State the blood parasite species.
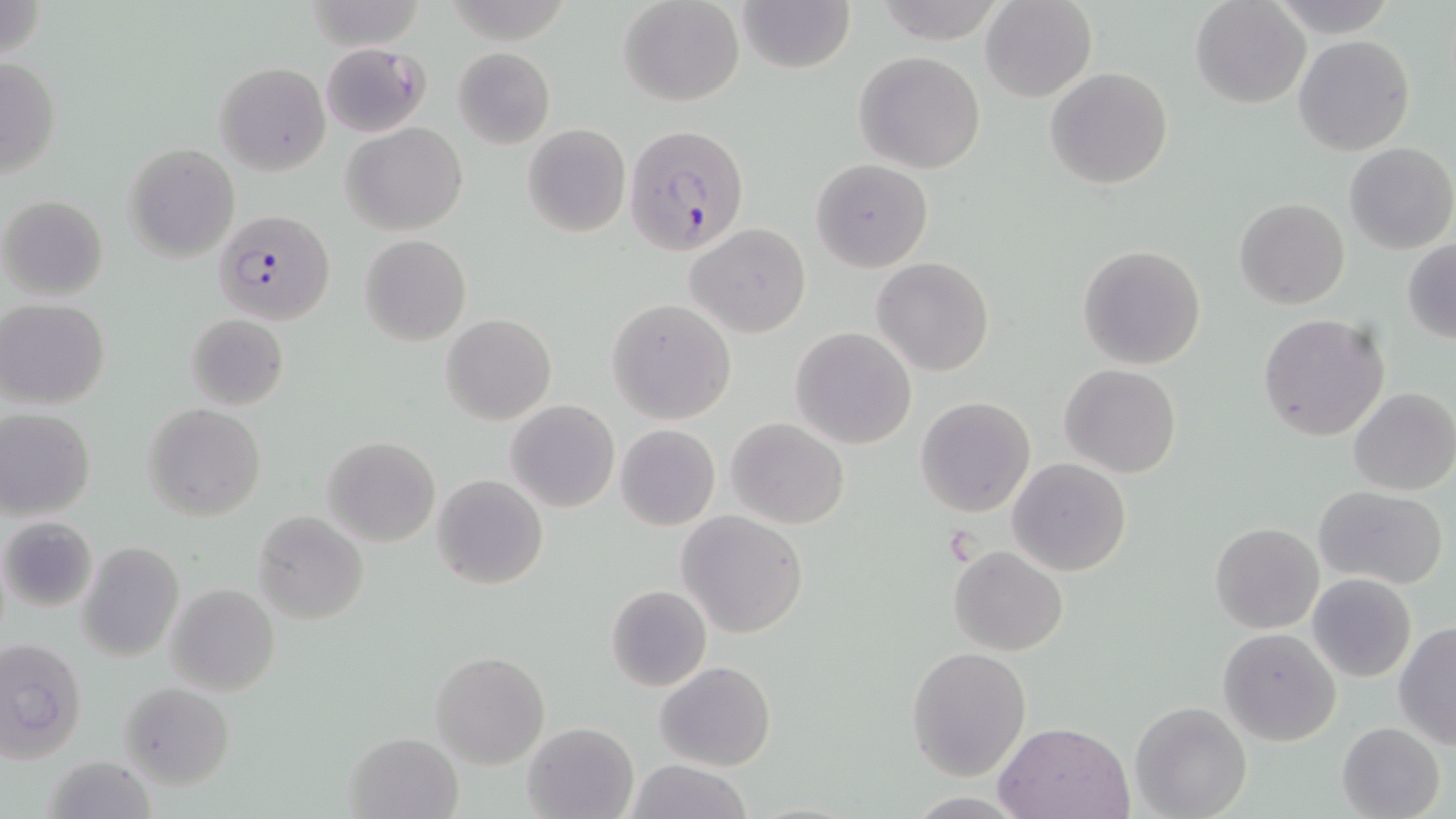
Plasmodium falciparum.

preparation = thin blood smear
Plasmodium falciparum-infected red blood cell locations = approximate bounding boxes as (x1,y1)-(x2,y2) corner pairs in pixels: (623,123)-(750,255), (216,210)-(334,325)
stain = May-Grünwald-Giemsa
image size = 1456×819 pixels
magnification = 1000x
modality = optical microscopy
field of view = one of a larger specimen
uninfected red blood cell locations = approximate bounding boxes as (x1,y1)-(x2,y2) corner pairs in pixels: (618,0)-(745,106), (736,0)-(855,73), (981,0)-(1098,102), (1190,0)-(1311,109), (1264,1)-(1403,35), (304,2)-(427,50), (1293,35)-(1414,156), (321,41)-(431,138), (453,47)-(555,148), (854,51)-(985,173), (0,56)-(61,177), (214,62)-(331,174), (1045,65)-(1173,189), (340,122)-(469,235), (522,124)-(630,237), (1343,141)-(1456,254), (123,144)-(240,262), (812,158)-(932,271), (1,195)-(108,301), (1233,198)-(1351,310), (687,223)-(810,338), (359,234)-(471,346), (1402,239)-(1456,343), (1077,243)-(1205,369), (872,257)-(995,376), (609,298)-(735,424), (1,299)-(110,410), (185,312)-(289,410), (1258,313)-(1390,441), (441,314)-(556,425), (790,327)-(916,449), (1060,363)-(1182,478), (1348,387)-(1456,496), (914,396)-(1036,516), (505,399)-(620,513), (143,402)-(267,523), (0,408)-(97,520), (727,417)-(849,529), (615,424)-(720,530), (322,435)-(441,547), (1008,459)-(1131,575), (431,474)-(549,590), (1313,486)-(1449,589), (252,510)-(369,626), (677,511)-(809,638), (2,517)-(96,611), (1210,522)-(1325,633), (78,542)-(184,662), (949,545)-(1068,656), (1308,574)-(1416,681), (165,583)-(279,698), (606,584)-(712,693), (1392,622)-(1456,750), (1217,627)-(1342,747), (0,638)-(86,761), (906,645)-(1033,780), (430,650)-(549,769), (655,660)-(776,770), (118,681)-(235,788), (1130,701)-(1253,819), (995,719)-(1137,818), (522,721)-(639,819), (1336,722)-(1446,819), (344,730)-(463,818), (40,756)-(160,818), (622,760)-(753,818)